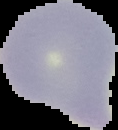
Summary:
  - Result: negative for malaria parasites
  - Preparation: thin blood film
  - Image type: segmented cell region on a black background
  - Image size: 118×130 pixels